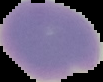

image type = segmented cell region on a black background
preparation = thin blood film
result = negative for malaria parasites
image size = 103×82 pixels